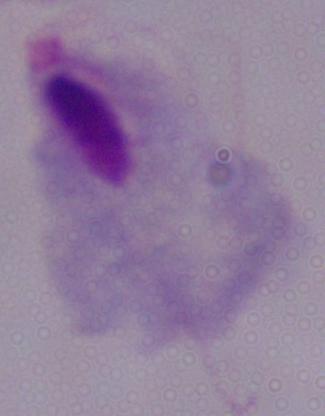
A trichomonad is shown. Captured at 1000x magnification. Photomicrograph.